Identify the parasite.
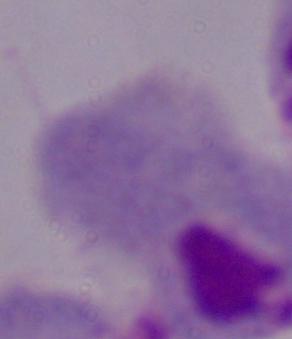

A trichomonad.

Captured at 1000x magnification. Photomicrograph.